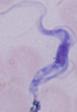

Photomicrograph. A trypanosome is shown. 1000x magnification.